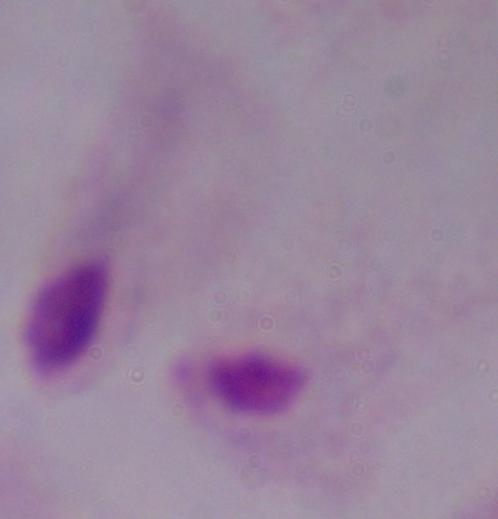
Summary:
  - Magnification: 1000x
  - Identification: trichomonad
  - Modality: micrograph